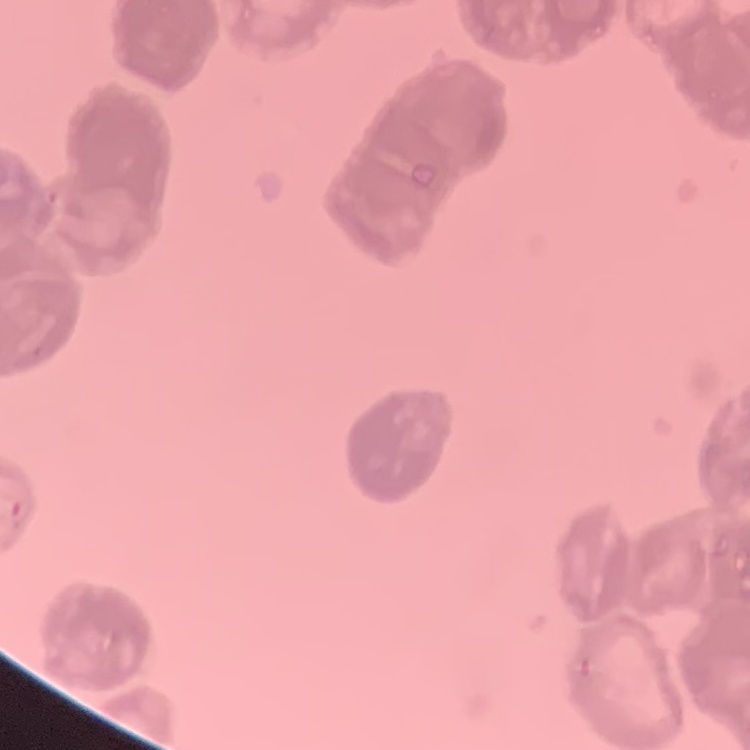
The red blood cells show rouleaux formation. Thin peripheral smear. Square crop of a larger photomicrograph. Field's or Giemsa stain.